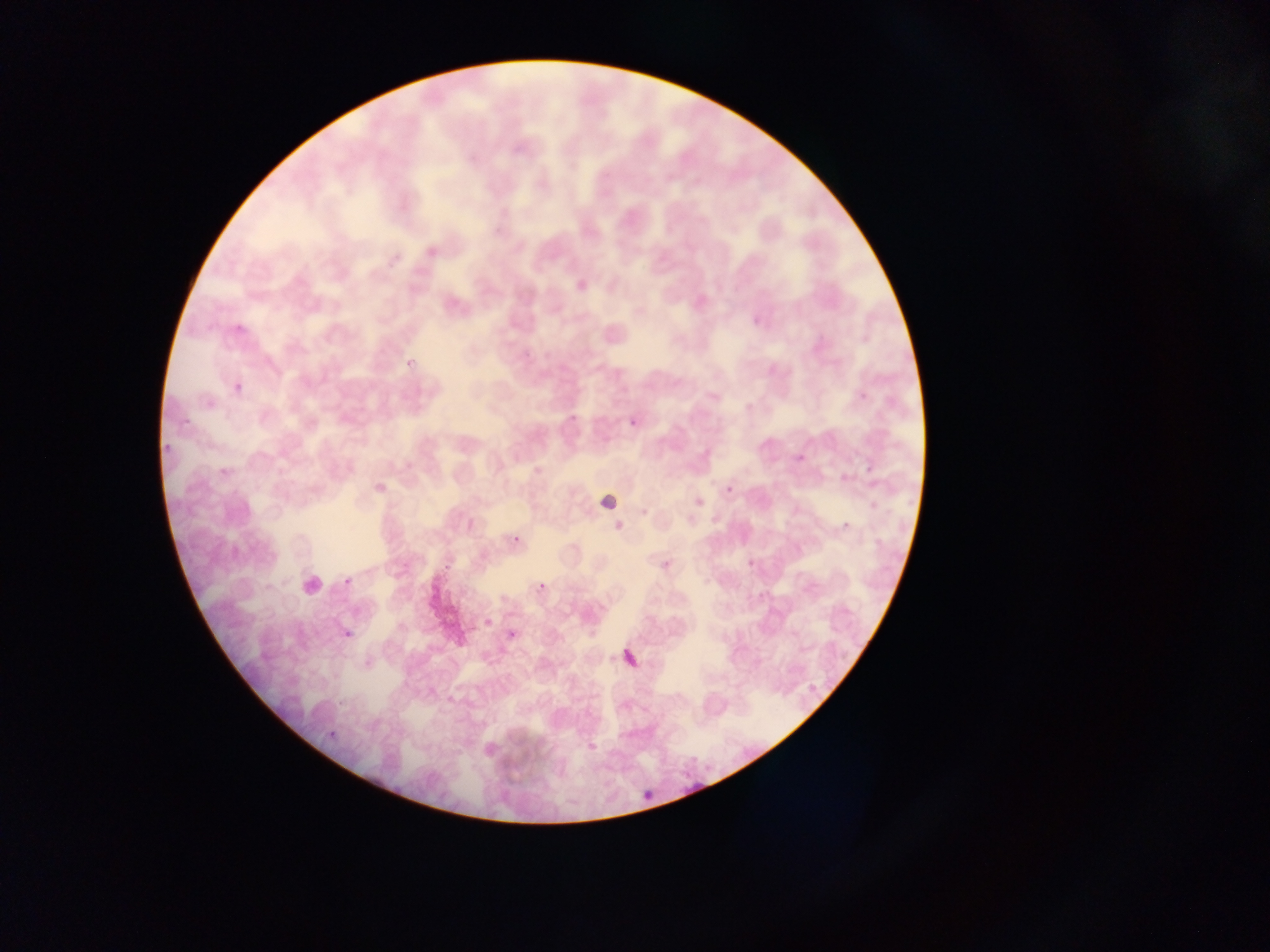 Approximate bounding boxes as (left, top, right, bottom) in pixels. Malaria parasite locations: (623, 412, 646, 438), (838, 516, 858, 538), (510, 532, 525, 548), (657, 555, 676, 575), (339, 572, 359, 592), (536, 579, 549, 596), (338, 624, 357, 644), (504, 625, 522, 644), (617, 643, 647, 675), (639, 786, 660, 809). Leukocyte locations: (596, 488, 623, 516), (294, 567, 331, 603). Artifact (stain precipitate or debris) locations: (425, 569, 467, 655). Thin blood smear. Image is 1270×952 pixels. Collected in Ghana. Single field of view. Mobile-phone photograph taken through the microscope.